Classify this cell by malaria status.
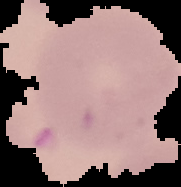
Uninfected.

preparation = thin blood smear
image size = 181×187 pixels
image type = cell region segmented out of the field of view; surrounding area masked to black